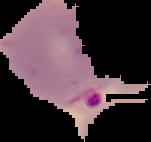

image type = cell region segmented out of the field of view; surrounding area masked to black
image size = 151×142 pixels
result = Plasmodium parasites detected
preparation = thin blood film